State the preparation type.
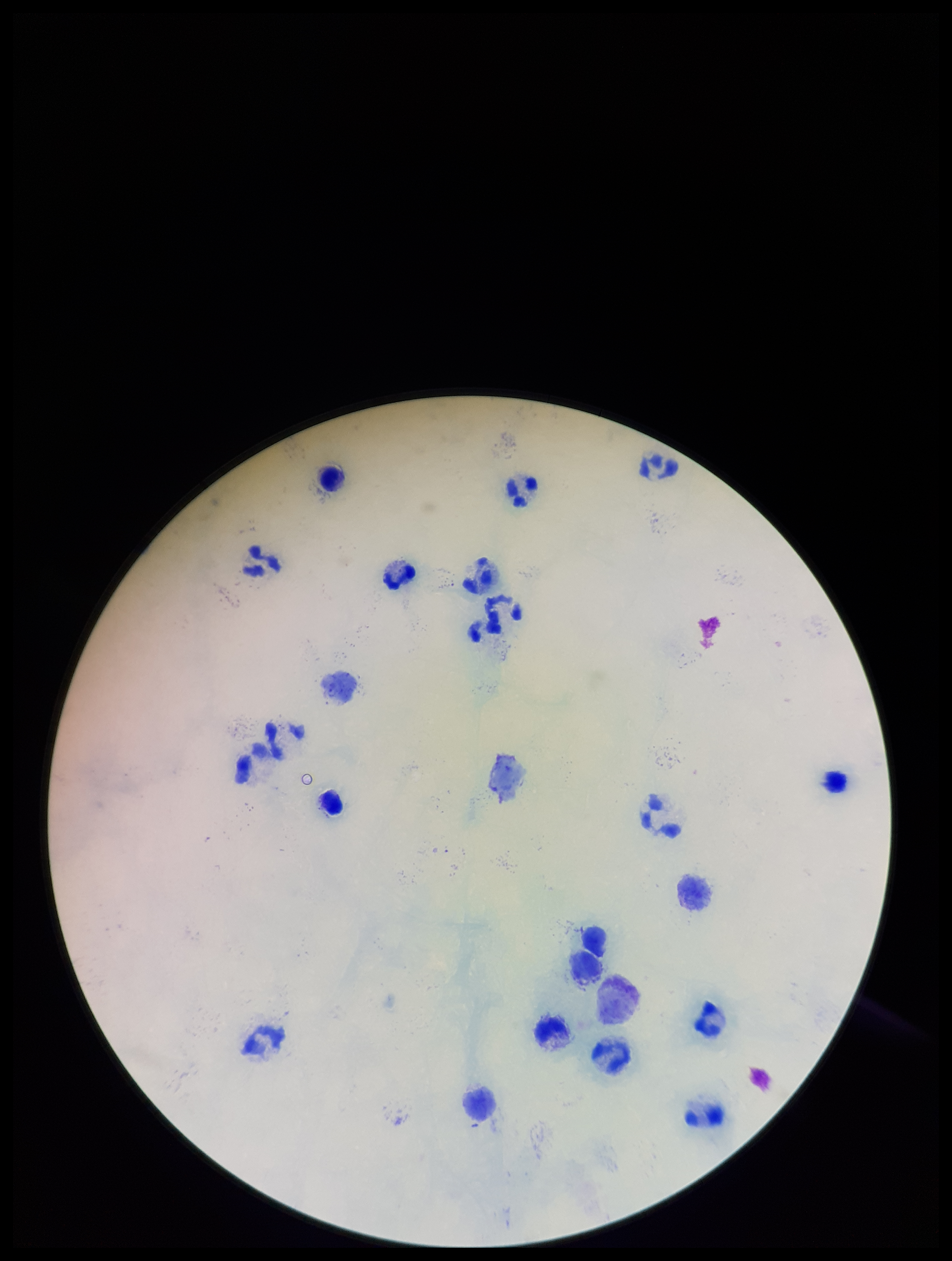
It is a thick blood smear.

{
  "image_size": "952×1261 pixels",
  "capture": "smartphone photograph through the microscope eyepiece",
  "field_of_view": "one from this slide",
  "stain": "Giemsa",
  "leukocyte_count": 20,
  "plasmodium_parasites": "none seen",
  "patient_malaria_status": "negative",
  "parasite_count": 0
}